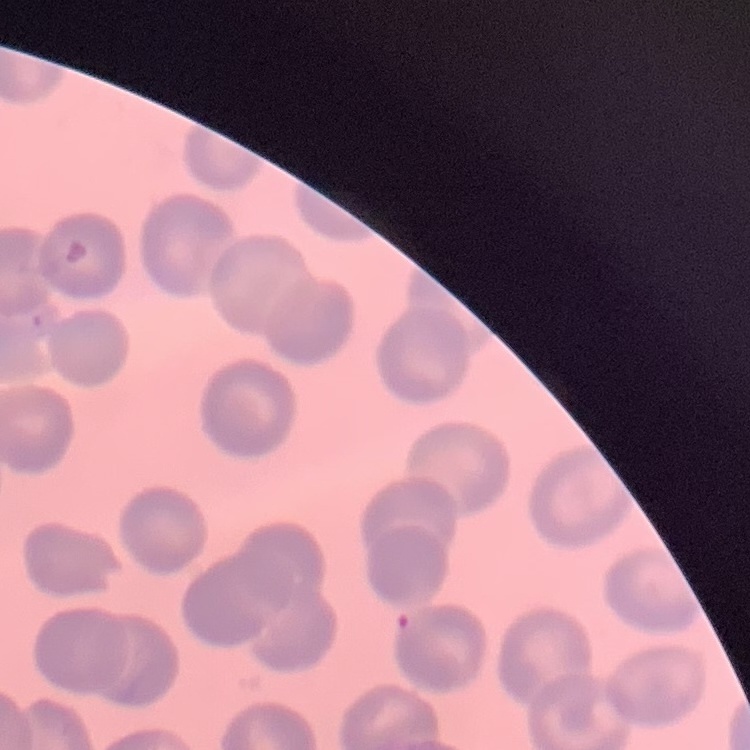
red_blood_cell_morphology: no rouleaux formation
image_type: square crop of a larger photomicrograph
preparation: thin blood smear
stain: Field's or Giemsa